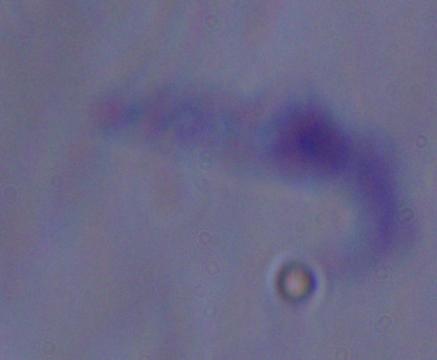
Summary:
  - Magnification: 1000x
  - Modality: micrograph
  - Identification: trypanosome